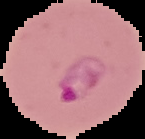 The area outside the segmented cell region is set to black. Image is 145×139 pixels. Malaria status: parasitized. From a thin blood smear.